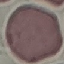

result = no malaria parasites detected
stain = Giemsa
capture = smartphone through the microscope eyepiece
preparation = thin blood smear
image type = cell patch, automatically extracted from a larger field of view and resized to 64 × 64 pixels